Report the malaria status of this cell.
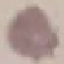
Uninfected.

{
  "preparation": "thin blood smear",
  "image_type": "cell patch, automatically extracted from a larger field of view and resized to 64 × 64 pixels",
  "capture": "smartphone through the microscope eyepiece",
  "stain": "Giemsa"
}